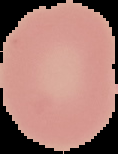
image_type: segmented cell region on a black background
preparation: thin blood film
result: no Plasmodium parasites seen
image_size: 118×154 pixels